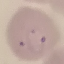

result = malaria parasites identified
capture = smartphone through the microscope eyepiece
preparation = thin blood smear
image type = cell patch, automatically extracted from a larger field of view and resized to 64 × 64 pixels
stain = Giemsa